Give the preparation type.
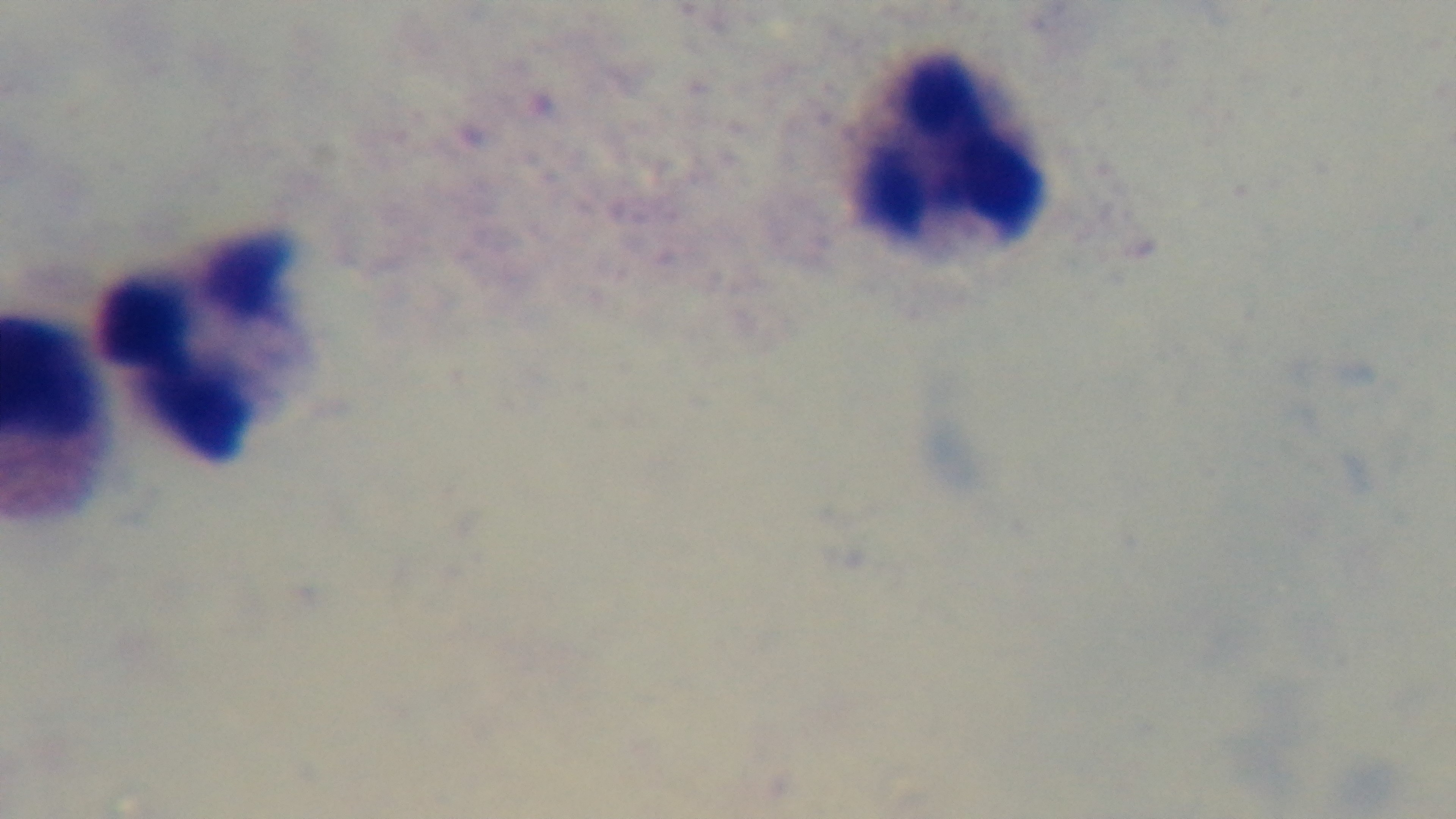

A thick smear.

Giemsa stain. Mounted 4K digital camera. 100x oil-immersion objective. Light microscopy. Malaria status: uninfected. One field from the slide.